Classify this cell by malaria status.
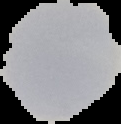

Uninfected.

preparation = thin blood smear
image type = segmented cell region on a black background
image size = 121×124 pixels